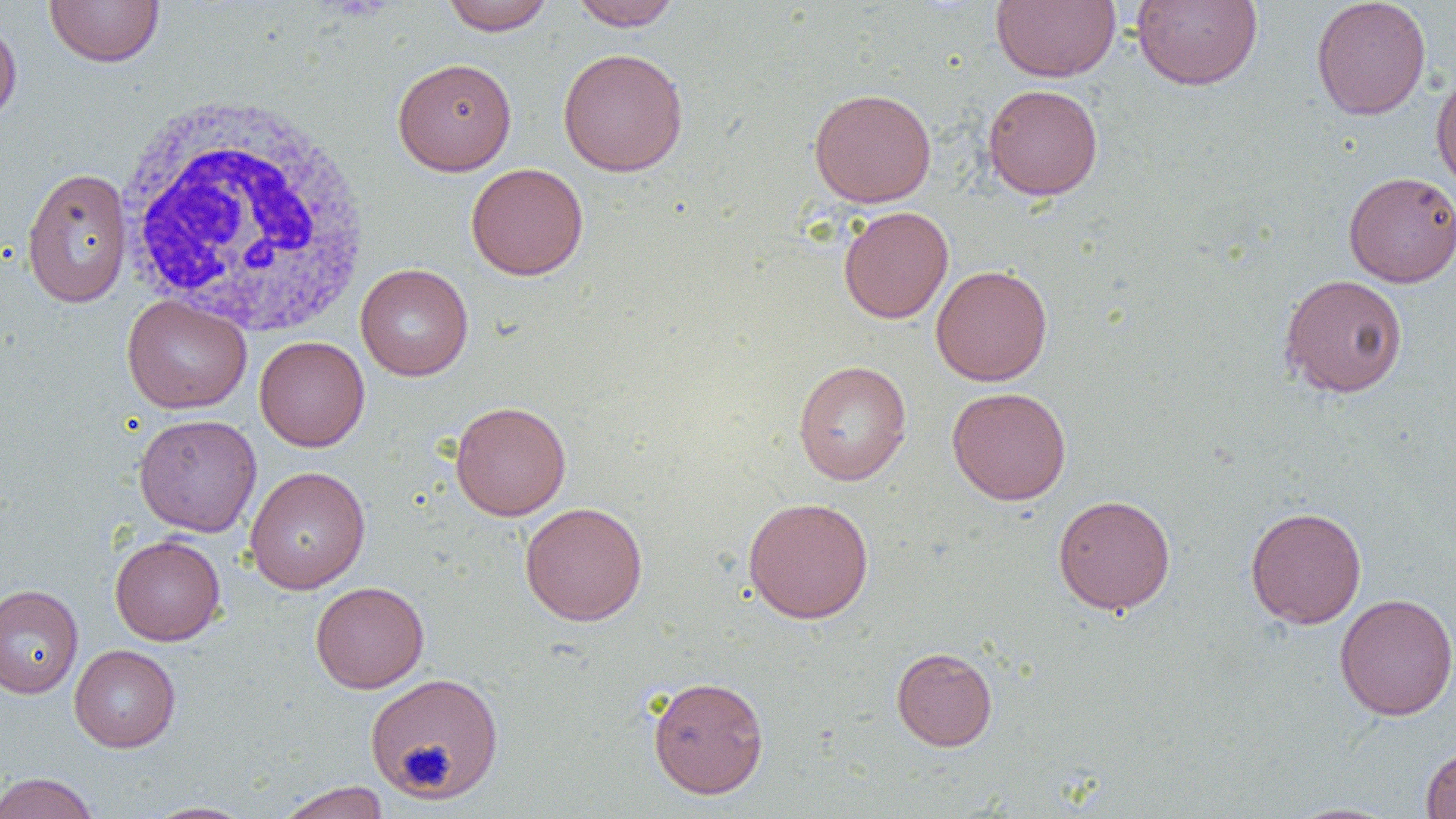
Approximate bounding boxes as [x1, y1, x2, y2] in pixels. White blood cell locations: [113, 89, 373, 338]. Platelet locations: [399, 743, 449, 792]. Uninfected red blood cell locations: [44, 0, 164, 67], [441, 0, 555, 35], [568, 0, 682, 30], [991, 0, 1120, 82], [1131, 0, 1263, 90], [1311, 0, 1431, 120], [0, 15, 22, 128], [557, 47, 689, 177], [392, 58, 518, 175], [1431, 66, 1456, 197], [983, 83, 1103, 200], [808, 87, 937, 208], [466, 162, 588, 280], [21, 167, 133, 307], [1343, 170, 1456, 287], [838, 206, 953, 324], [355, 264, 473, 381], [931, 264, 1052, 386], [1278, 273, 1409, 398], [122, 295, 252, 414], [254, 336, 370, 451], [793, 360, 911, 485], [947, 387, 1071, 505], [450, 401, 571, 521], [133, 413, 262, 537], [244, 465, 371, 594], [1052, 494, 1176, 614], [743, 496, 874, 623], [520, 501, 648, 626], [1245, 506, 1367, 629], [110, 534, 225, 646], [310, 581, 429, 693], [0, 584, 83, 699], [1334, 593, 1456, 721], [69, 644, 180, 752], [891, 646, 997, 751], [365, 673, 504, 801], [648, 675, 769, 798], [1420, 743, 1456, 818], [0, 772, 100, 818], [275, 781, 391, 819], [142, 801, 258, 818], [1281, 802, 1404, 819]. Slide-level diagnosis: no evidence of blood parasites. Light microscopy. Thin blood film. 1000x magnification. One field of a larger specimen. Image is 1456×819 pixels.